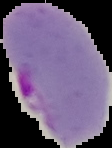
malaria status = parasitized
image type = segmented cell region on a black background
image size = 112×148 pixels
preparation = thin blood smear